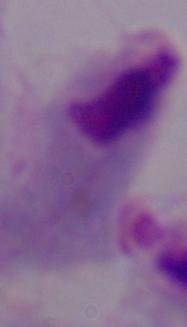 Captured at 1000x magnification. A trichomonad is seen. Micrograph.